Report the malaria status of this cell.
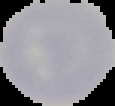
It is uninfected.

{
  "preparation": "thin blood smear",
  "image_type": "segmented cell region on a black background",
  "image_size": "115×106 pixels"
}